Classify this cell by malaria status.
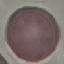

Uninfected.

Summary:
  - Stain: Giemsa
  - Capture: smartphone through the microscope eyepiece
  - Image type: cell patch, automatically extracted from a larger field of view and resized to 64 × 64 pixels
  - Preparation: thin smear